Assess this cell for malaria.
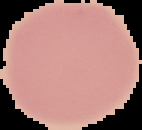
Uninfected.

Summary:
  - Image size: 142×130 pixels
  - Image type: segmented cell region with the area outside set to black
  - Preparation: thin blood smear